Evaluate for Plasmodium parasites.
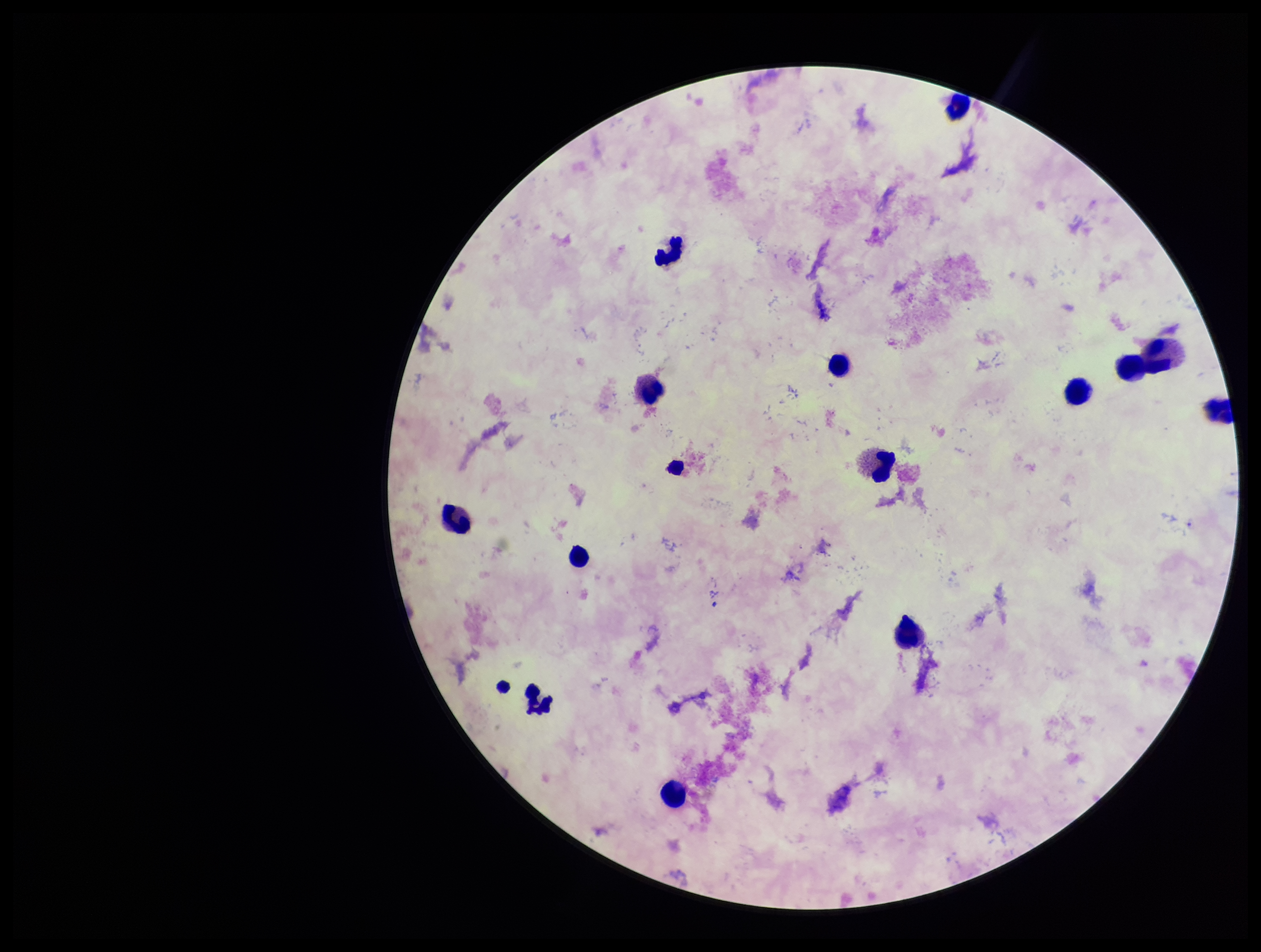
None identified.

species reported for this patient = Plasmodium falciparum
stain = Giemsa
image size = 1261×952 pixels
preparation = thick smear
capture = smartphone photograph through the microscope eyepiece
field of view = one from this slide
leukocyte count = 14
parasite count = 0
patient malaria status = positive